Identify the parasite.
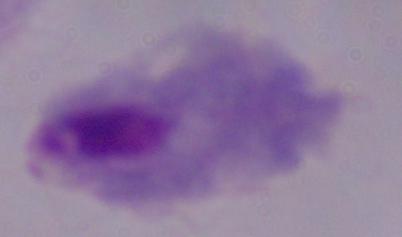

A trichomonad.

Summary:
  - Modality: micrograph
  - Magnification: 1000x